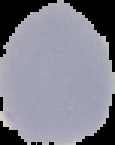

Summary:
  - Preparation: thin blood film
  - Image size: 115×145 pixels
  - Image type: segmented cell region with the area outside set to black
  - Malaria status: uninfected